Classify this cell by malaria status.
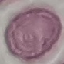
Uninfected.

{
  "image_type": "automatically extracted cell patch, resized to 64 × 64 pixels",
  "stain": "Giemsa",
  "capture": "smartphone through the microscope eyepiece",
  "preparation": "thin smear"
}